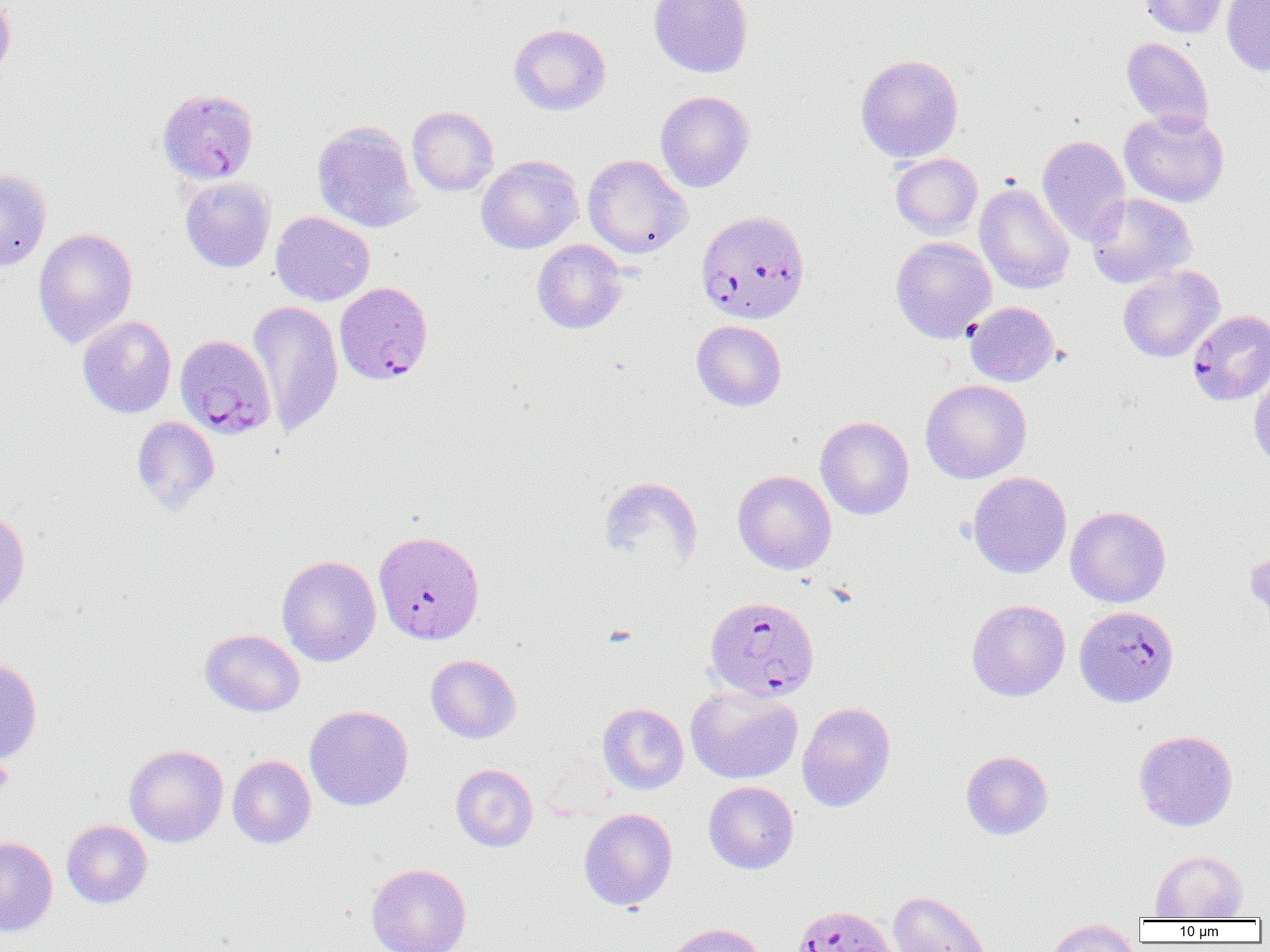
Approximate bounding boxes as (x1, y1, x2, y2) in pixels. Platelet locations: (0, 757, 14, 794). Uninfected red blood cell locations: (0, 0, 16, 83), (648, 0, 754, 78), (1138, 0, 1229, 38), (1221, 0, 1270, 76), (509, 23, 611, 115), (1121, 37, 1215, 132), (855, 54, 964, 163), (655, 91, 755, 192), (407, 106, 499, 196), (1119, 109, 1229, 207), (312, 121, 422, 233), (1037, 135, 1131, 246), (890, 153, 983, 240), (583, 154, 692, 258), (476, 156, 584, 254), (0, 167, 52, 271), (180, 176, 276, 272), (974, 183, 1074, 294), (1085, 193, 1197, 288), (270, 211, 375, 306), (33, 227, 138, 348), (890, 236, 997, 343), (532, 239, 628, 333), (1117, 265, 1224, 363), (248, 300, 343, 438), (965, 301, 1059, 386), (77, 315, 177, 418), (691, 320, 787, 411), (1248, 370, 1270, 472), (921, 379, 1032, 483), (131, 416, 220, 514), (815, 416, 914, 520), (733, 470, 837, 575), (967, 471, 1072, 579), (598, 477, 703, 570), (0, 504, 30, 617), (1065, 506, 1171, 607), (1245, 545, 1270, 635), (277, 555, 381, 666), (966, 599, 1070, 701), (200, 628, 305, 716), (426, 654, 521, 743), (0, 656, 43, 765), (686, 685, 803, 785), (797, 701, 896, 812), (597, 703, 689, 794), (305, 705, 413, 811), (1133, 729, 1238, 831), (124, 744, 228, 847), (961, 750, 1053, 839), (227, 755, 316, 848), (451, 763, 538, 852), (703, 781, 799, 874), (579, 807, 678, 910), (61, 820, 152, 908), (0, 836, 58, 937), (1150, 851, 1247, 919), (366, 863, 471, 952), (887, 889, 994, 952), (1047, 919, 1140, 952), (662, 922, 767, 952). Plasmodium falciparum-infected red blood cell locations: (157, 88, 259, 184), (696, 209, 810, 325), (334, 281, 433, 385), (1187, 309, 1270, 406), (175, 335, 276, 440), (373, 530, 486, 645), (704, 596, 820, 702), (1074, 605, 1178, 707), (791, 903, 899, 951). Slide-level diagnosis: Plasmodium falciparum. 1000x magnification. Single field of view. Light microscopy. Image is 1270×952 pixels. Thin blood film.